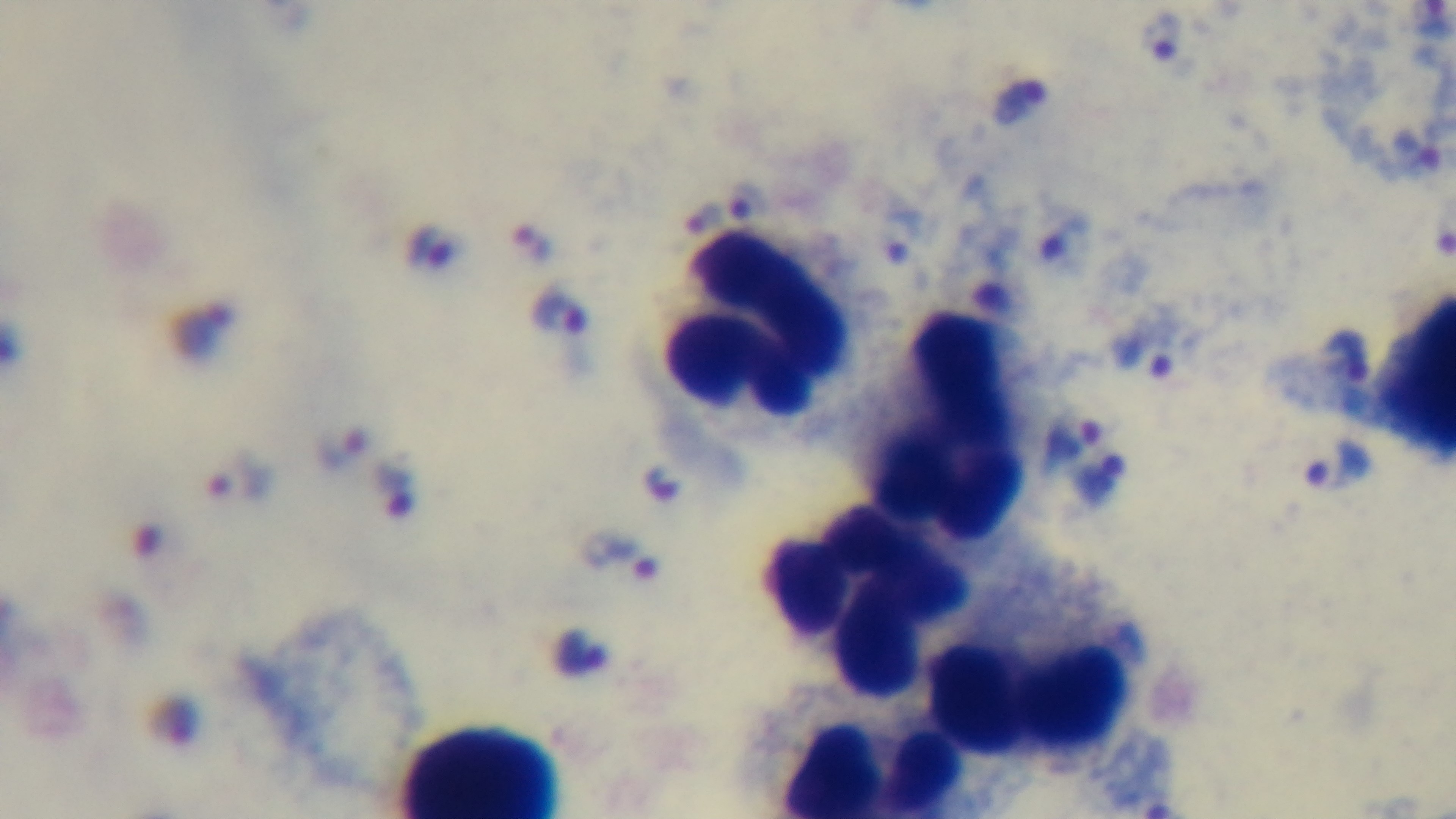

100x oil-immersion objective. Malaria status: infected. Light microscopy. Giemsa stain. Preparation: thick. Mounted 4K digital camera. One field from the slide.